Classify this cell by malaria status.
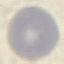
It is uninfected.

Giemsa stain. Acquired by smartphone through the microscope eyepiece. Cell patch, automatically extracted from a larger field of view and resized to 64 × 64 pixels. Thin blood smear.